Report the malaria status of this cell.
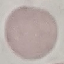

Uninfected.

Summary:
  - Capture: smartphone camera at the microscope eyepiece
  - Image type: automatically extracted cell patch, resized to 64 × 64 pixels
  - Preparation: thin smear
  - Stain: Giemsa